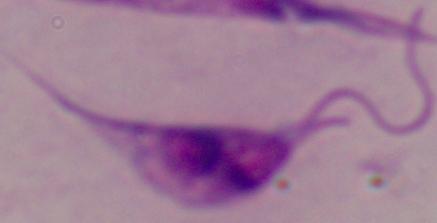 A Leishmania parasite is seen. Captured at 1000x magnification. Photomicrograph.